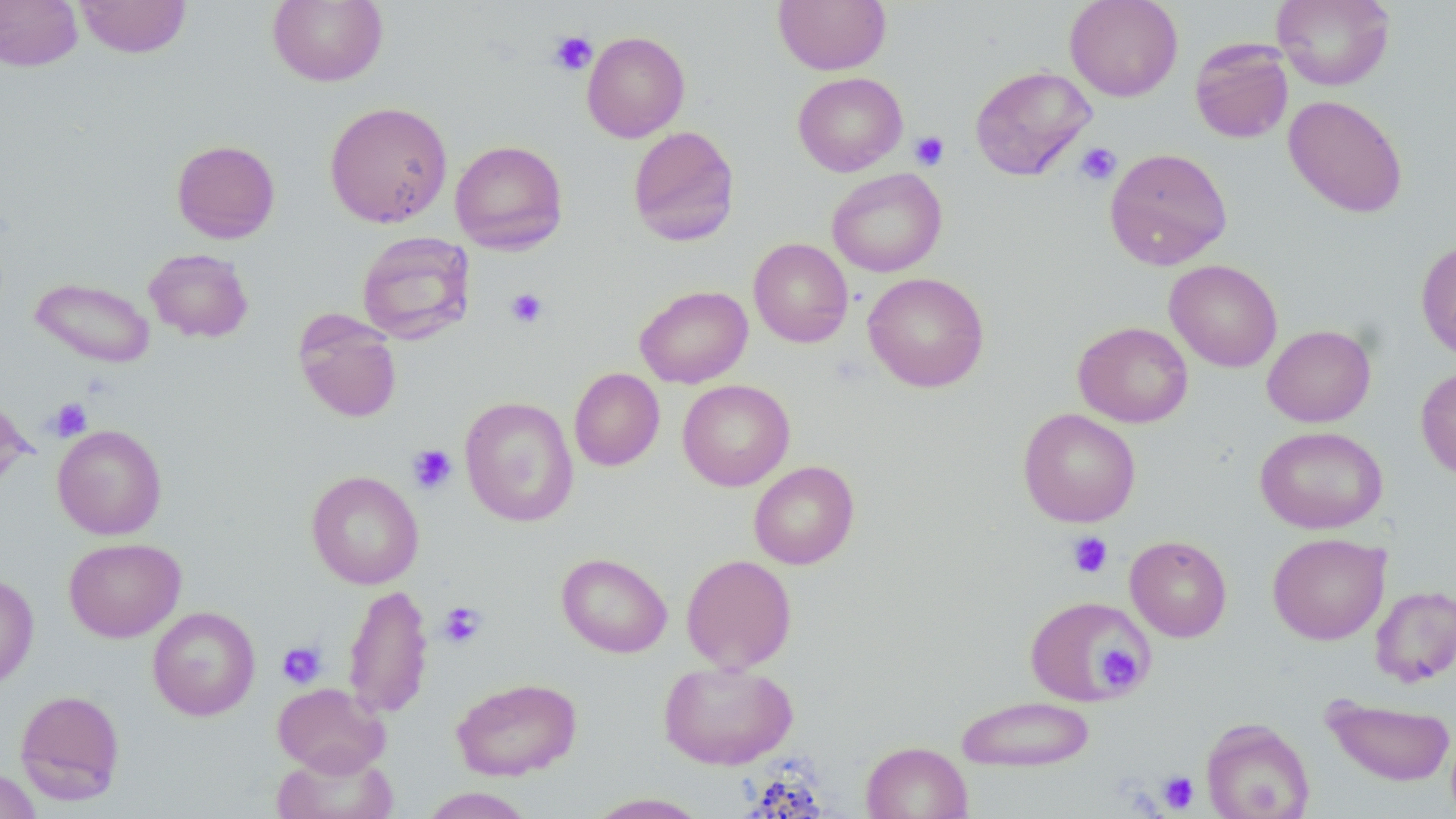
Approximate bounding boxes as (x1,y1)-(x2,y2) corner pairs in pixels. Platelet locations: (548,30)-(597,76), (910,131)-(949,171), (1075,142)-(1122,186), (506,288)-(549,329), (47,397)-(92,441), (407,444)-(457,495), (1066,531)-(1113,578), (438,602)-(487,649), (276,641)-(327,689), (1097,644)-(1142,688), (1157,770)-(1199,814). Uninfected red blood cell locations: (0,0)-(83,71), (75,0)-(192,58), (267,0)-(388,87), (1065,0)-(1183,101), (1272,0)-(1395,90), (774,1)-(891,74), (582,31)-(690,142), (1189,38)-(1294,144), (970,65)-(1096,181), (793,72)-(907,176), (1284,95)-(1408,218), (324,101)-(453,228), (627,125)-(740,246), (171,139)-(280,243), (450,139)-(568,254), (1105,147)-(1232,270), (827,168)-(947,277), (356,231)-(475,344), (748,238)-(853,347), (1415,240)-(1456,361), (143,248)-(254,343), (1165,259)-(1282,372), (863,272)-(989,392), (30,277)-(155,368), (635,285)-(753,388), (294,312)-(403,423), (1073,322)-(1193,428), (1262,324)-(1375,427), (1415,365)-(1456,482), (569,367)-(664,471), (678,379)-(794,491), (459,396)-(579,526), (1018,408)-(1141,527), (52,424)-(167,539), (1255,426)-(1388,534), (749,461)-(859,569), (306,470)-(424,589), (1267,533)-(1390,644), (1125,535)-(1232,642), (63,537)-(186,642), (557,552)-(672,658), (681,554)-(797,673), (0,573)-(38,690), (343,584)-(433,718), (1370,585)-(1456,686), (1025,595)-(1152,706), (147,606)-(261,721), (658,660)-(798,769), (451,677)-(582,780), (272,682)-(390,777), (15,689)-(126,804), (956,695)-(1095,772), (1323,696)-(1455,786), (1201,718)-(1315,819), (861,741)-(972,819), (272,747)-(397,819), (0,767)-(42,819), (420,787)-(534,818), (585,792)-(711,818). Slide-level diagnosis: no evidence of blood parasites. Image is 1456×819 pixels. May-Grünwald-Giemsa stain. Single field of view. Thin blood smear. Optical microscopy. Captured at 1000x magnification.